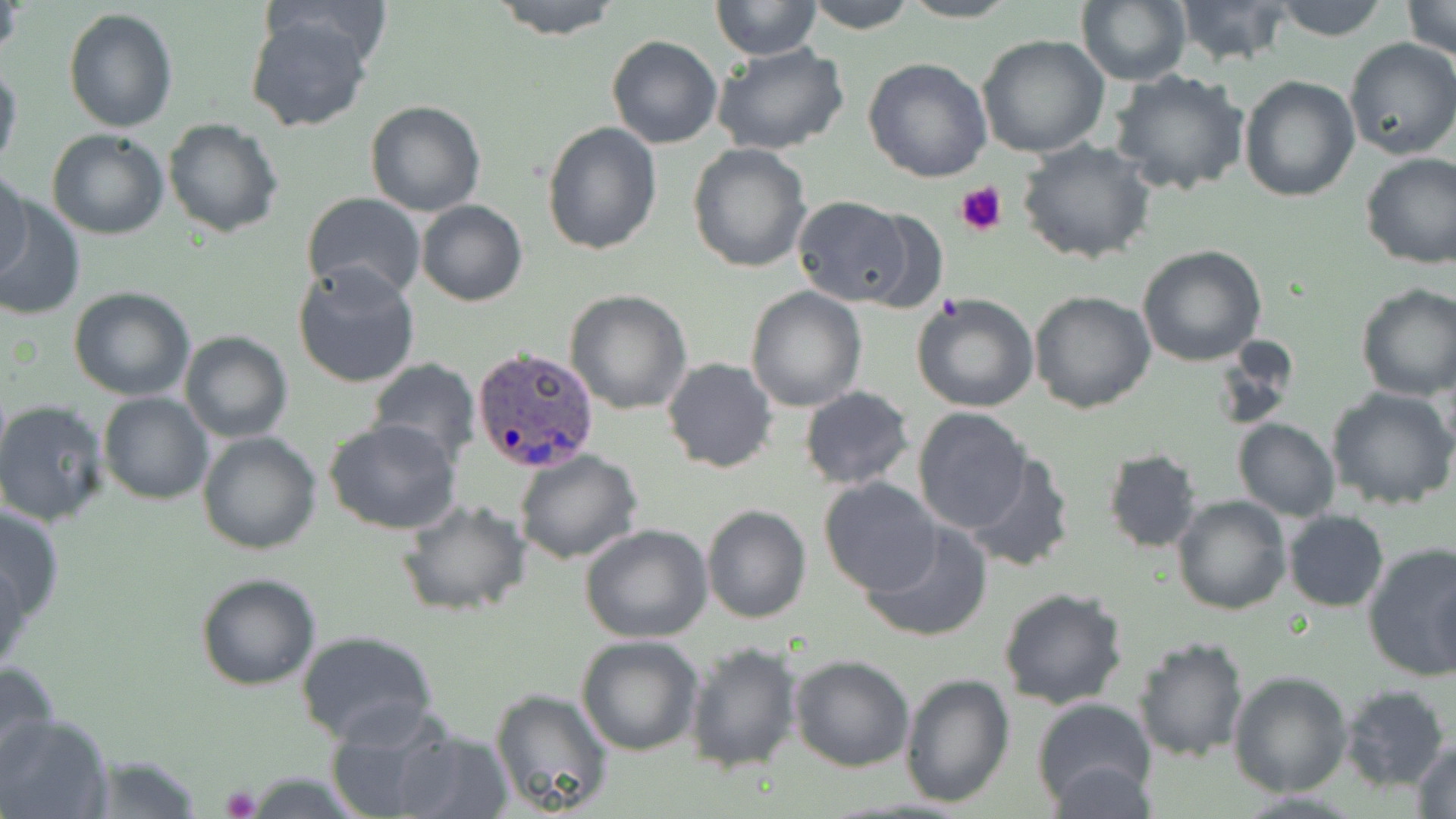

Summary:
  - Coordinate format: approximate bounding boxes as named x1/y1/x2/y2 corners in pixels
  - Plasmodium ovale-infected red blood cell locations: (x1=471, y1=347, x2=599, y2=473)
  - Uninfected red blood cell locations: (x1=488, y1=0, x2=624, y2=40), (x1=711, y1=0, x2=824, y2=59), (x1=802, y1=0, x2=918, y2=34), (x1=899, y1=0, x2=1022, y2=23), (x1=1078, y1=0, x2=1191, y2=86), (x1=1174, y1=0, x2=1296, y2=68), (x1=1269, y1=0, x2=1390, y2=42), (x1=1402, y1=0, x2=1456, y2=61), (x1=1, y1=1, x2=25, y2=66), (x1=63, y1=7, x2=178, y2=133), (x1=245, y1=12, x2=378, y2=134), (x1=605, y1=34, x2=722, y2=149), (x1=976, y1=34, x2=1110, y2=158), (x1=1344, y1=37, x2=1456, y2=160), (x1=712, y1=43, x2=850, y2=156), (x1=863, y1=56, x2=992, y2=182), (x1=0, y1=57, x2=23, y2=177), (x1=1109, y1=68, x2=1252, y2=196), (x1=1240, y1=76, x2=1361, y2=204), (x1=365, y1=100, x2=486, y2=218), (x1=163, y1=119, x2=284, y2=238), (x1=541, y1=122, x2=662, y2=256), (x1=46, y1=129, x2=170, y2=240), (x1=1018, y1=139, x2=1154, y2=264), (x1=687, y1=144, x2=812, y2=273), (x1=1360, y1=153, x2=1456, y2=271), (x1=0, y1=167, x2=33, y2=283), (x1=300, y1=193, x2=427, y2=301), (x1=1, y1=195, x2=85, y2=321), (x1=790, y1=198, x2=916, y2=307), (x1=416, y1=201, x2=528, y2=306), (x1=843, y1=207, x2=951, y2=314), (x1=1137, y1=245, x2=1267, y2=367), (x1=291, y1=261, x2=421, y2=389), (x1=1355, y1=283, x2=1456, y2=400), (x1=745, y1=286, x2=868, y2=411), (x1=68, y1=287, x2=195, y2=401), (x1=564, y1=289, x2=693, y2=413), (x1=1028, y1=290, x2=1156, y2=413), (x1=911, y1=292, x2=1039, y2=412), (x1=179, y1=331, x2=294, y2=443), (x1=366, y1=357, x2=481, y2=463), (x1=662, y1=357, x2=779, y2=474), (x1=798, y1=386, x2=916, y2=491), (x1=1326, y1=386, x2=1456, y2=512), (x1=98, y1=392, x2=214, y2=506), (x1=0, y1=399, x2=110, y2=527), (x1=913, y1=407, x2=1030, y2=534), (x1=321, y1=419, x2=462, y2=536), (x1=1233, y1=419, x2=1340, y2=520), (x1=197, y1=430, x2=322, y2=554), (x1=1102, y1=447, x2=1204, y2=553), (x1=513, y1=449, x2=642, y2=564), (x1=963, y1=452, x2=1075, y2=574), (x1=818, y1=477, x2=944, y2=597), (x1=1171, y1=495, x2=1291, y2=617), (x1=393, y1=497, x2=534, y2=620), (x1=0, y1=503, x2=65, y2=625), (x1=701, y1=504, x2=812, y2=624), (x1=1283, y1=510, x2=1389, y2=612), (x1=860, y1=520, x2=995, y2=643), (x1=579, y1=525, x2=713, y2=644), (x1=1360, y1=542, x2=1456, y2=684), (x1=0, y1=553, x2=29, y2=681), (x1=195, y1=572, x2=322, y2=691), (x1=998, y1=587, x2=1130, y2=711), (x1=294, y1=629, x2=439, y2=745), (x1=576, y1=634, x2=705, y2=756), (x1=1132, y1=636, x2=1248, y2=762), (x1=685, y1=641, x2=801, y2=774), (x1=789, y1=655, x2=914, y2=772), (x1=0, y1=659, x2=62, y2=783), (x1=1228, y1=669, x2=1353, y2=797), (x1=899, y1=673, x2=1015, y2=808), (x1=1337, y1=684, x2=1450, y2=791), (x1=489, y1=687, x2=617, y2=819), (x1=1030, y1=696, x2=1160, y2=813), (x1=324, y1=704, x2=467, y2=819), (x1=0, y1=712, x2=112, y2=819), (x1=390, y1=728, x2=514, y2=818), (x1=1411, y1=739, x2=1456, y2=819), (x1=80, y1=754, x2=206, y2=818), (x1=1046, y1=761, x2=1160, y2=818), (x1=243, y1=773, x2=370, y2=815)
  - Platelet locations: (x1=955, y1=179, x2=1009, y2=236), (x1=220, y1=786, x2=260, y2=818)
  - Slide-level diagnosis: Plasmodium ovale
  - Stain: May-Grünwald-Giemsa
  - Image size: 1456×819 pixels
  - Field of view: one of a larger specimen
  - Magnification: 1000x
  - Modality: light microscopy
  - Preparation: thin blood film